Identify the parasite.
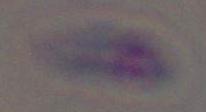

Toxoplasma gondii.

{
  "magnification": "1000x",
  "modality": "photomicrograph"
}